Assess this cell for malaria.
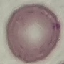

Uninfected.

image type = cell patch, automatically extracted from a larger field of view and resized to 64 × 64 pixels
preparation = thin smear
capture = smartphone camera at the microscope eyepiece
stain = Giemsa